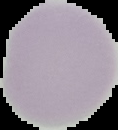
{
  "preparation": "thin blood smear",
  "malaria_status": "uninfected",
  "image_type": "segmented cell region with the area outside set to black",
  "image_size": "118×130 pixels"
}